Classify this cell by malaria status.
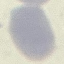
Uninfected.

Summary:
  - Preparation: thin smear
  - Capture: smartphone camera at the microscope eyepiece
  - Image type: cell patch, automatically extracted from a larger field of view and resized to 64 × 64 pixels
  - Stain: Giemsa